Name the parasite shown.
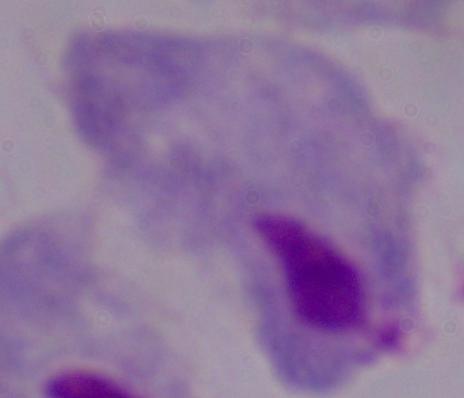
This is a trichomonad.

1000x magnification. Micrograph.